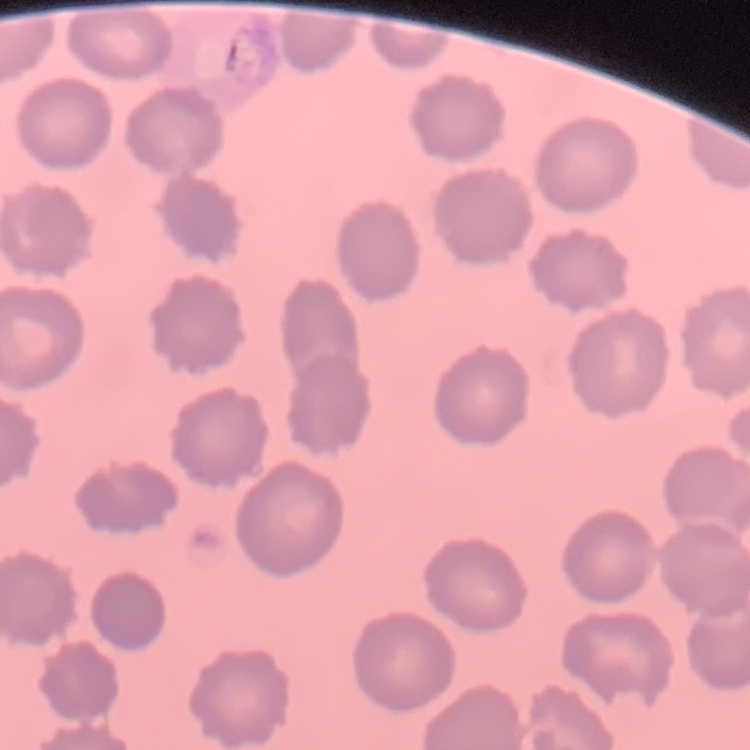

Summary:
  - Erythrocyte morphology: no rouleaux formation
  - Preparation: thin blood film
  - Stain: Field's or Giemsa
  - Image type: square crop of a larger photomicrograph